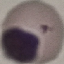
Malaria status: uninfected. Photographed with a smartphone camera at the microscope eyepiece. Cell patch, automatically extracted from a larger field of view and resized to 64 × 64 pixels. Giemsa-stained preparation. Thin blood smear.